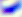
Summary:
  - Identification: Toxoplasma gondii
  - Modality: micrograph
  - Magnification: 400x